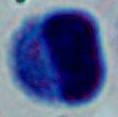
{
  "identification": "white blood cell",
  "magnification": "1000x",
  "modality": "micrograph"
}